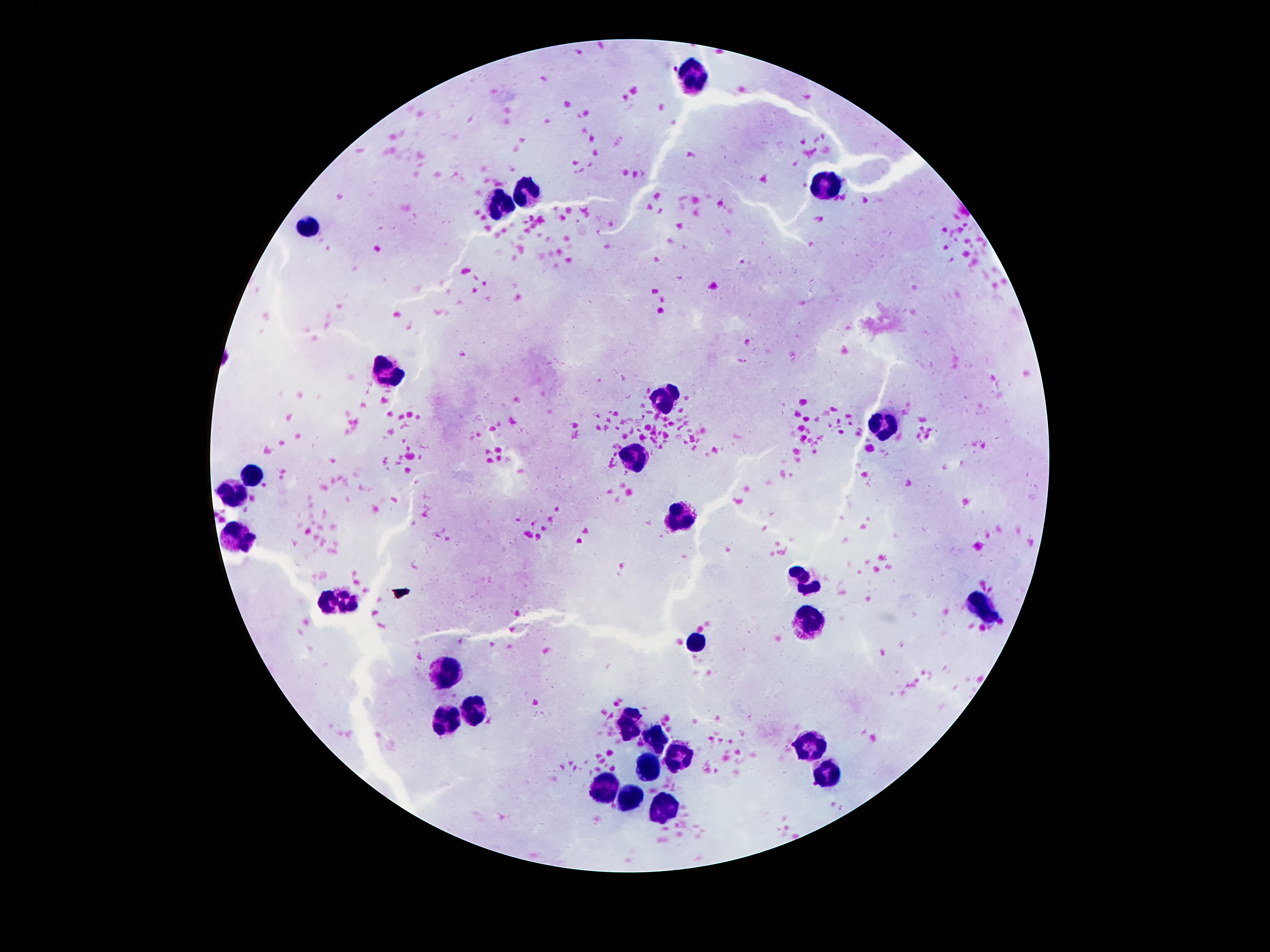 Approximate centers as {x, y} in pixels. Leukocyte locations: {693, 72}, {827, 188}, {530, 189}, {500, 206}, {309, 228}, {389, 373}, {661, 403}, {881, 421}, {639, 454}, {248, 477}, {235, 487}, {684, 517}, {239, 532}, {800, 576}, {339, 596}, {981, 611}, {811, 620}, {698, 640}, {443, 672}, {471, 714}, {632, 717}, {443, 721}, {661, 741}, {813, 743}, {684, 759}, {645, 769}, {829, 774}, {605, 791}, {632, 798}, {668, 810}. One field from this slide. Image is 1270×952 pixels. Patient malaria status: not infected. 100x magnification. Smartphone photograph taken through the microscope eyepiece. Giemsa stain. Thick peripheral-blood smear.